Assess for malaria.
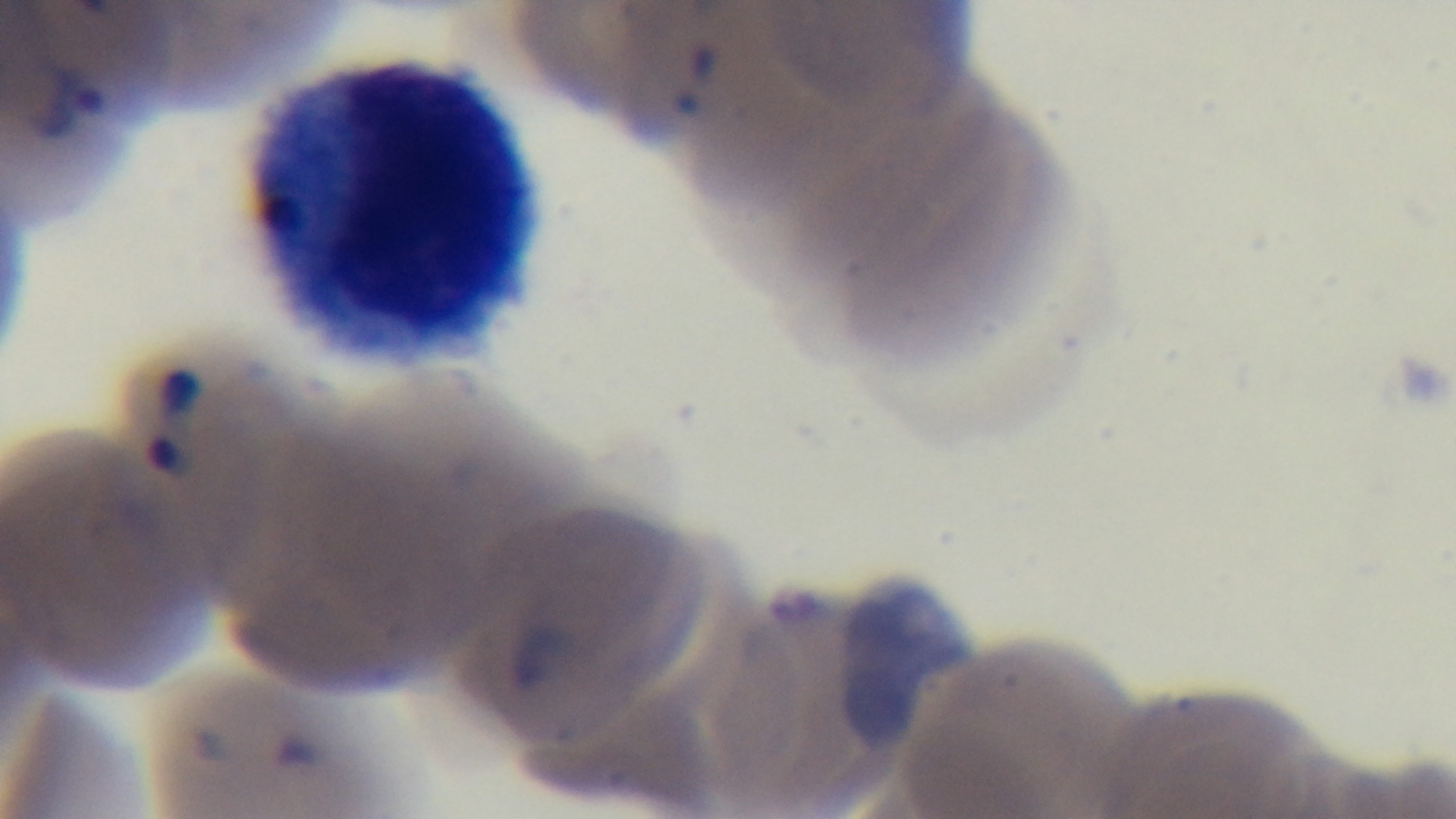

Infected.

Captured with a mounted 4K digital camera. Single field of view. Oil-immersion objective, 100x. Photomicrograph. Preparation: thin smear. Giemsa stain.